Outline each Plasmodium falciparum-infected red blood cell.
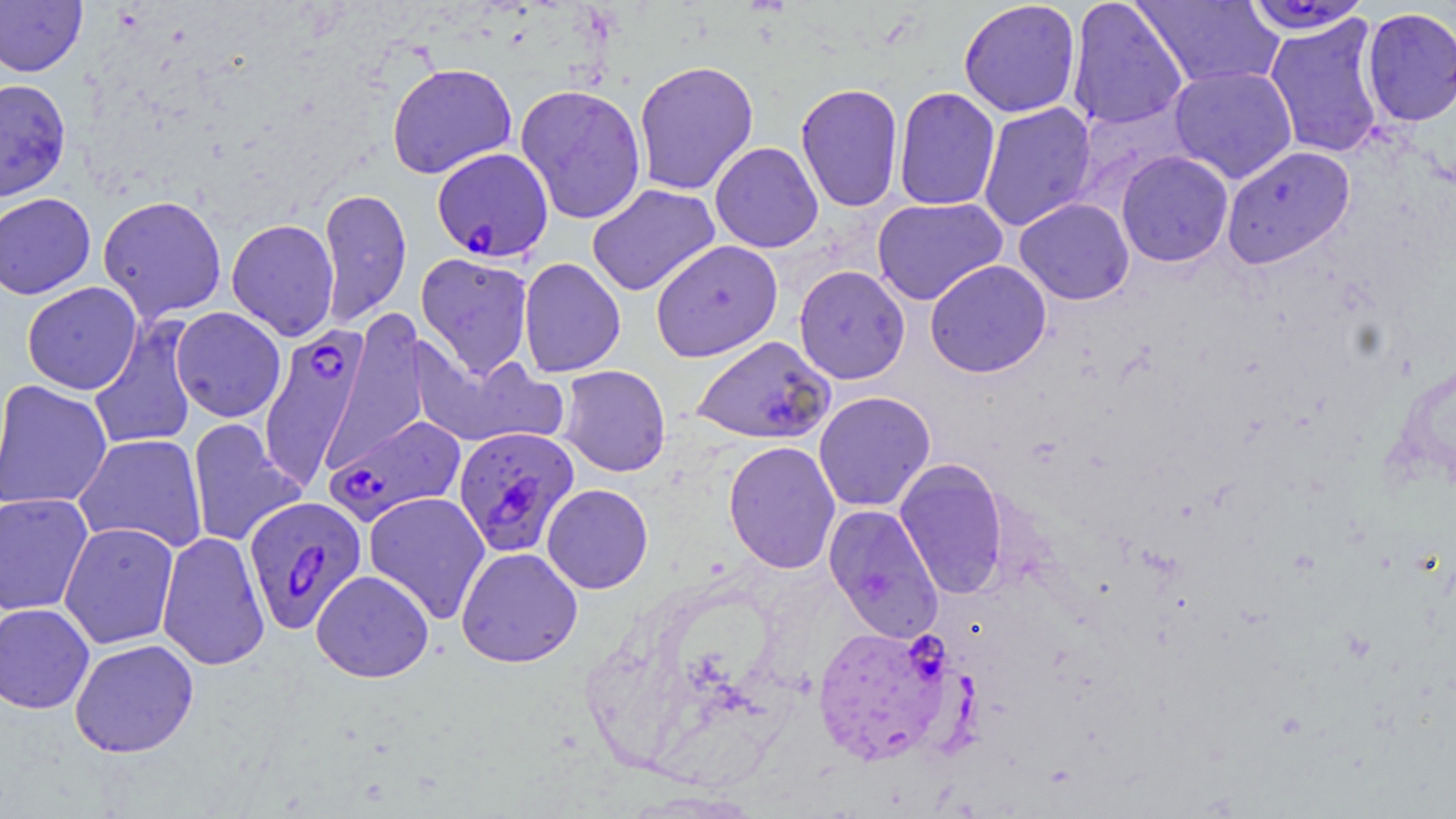

Approximate bounding boxes as named x1/y1/x2/y2 corners in pixels.
Plasmodium falciparum-infected red blood cells: (x1=432, y1=147, x2=554, y2=262), (x1=258, y1=321, x2=371, y2=485), (x1=690, y1=335, x2=835, y2=445), (x1=324, y1=413, x2=466, y2=527), (x1=453, y1=426, x2=580, y2=557), (x1=243, y1=495, x2=368, y2=634), (x1=812, y1=624, x2=954, y2=766).

slide_level_diagnosis: Plasmodium falciparum
image_size: 1456×819 pixels
modality: optical microscopy
uninfected_red_blood_cell_locations: 'approximate bounding boxes as named x1/y1/x2/y2 corners in pixels: (x1=958, y1=0, x2=1081, y2=118), (x1=1066, y1=0, x2=1188, y2=130), (x1=1132, y1=0, x2=1285, y2=89), (x1=0, y1=1, x2=87, y2=76), (x1=1240, y1=1, x2=1374, y2=36), (x1=1360, y1=7, x2=1456, y2=127), (x1=1263, y1=16, x2=1387, y2=158), (x1=633, y1=59, x2=759, y2=196), (x1=387, y1=63, x2=517, y2=179), (x1=1169, y1=66, x2=1297, y2=183), (x1=0, y1=78, x2=71, y2=202), (x1=795, y1=82, x2=903, y2=212), (x1=514, y1=84, x2=647, y2=225), (x1=893, y1=87, x2=1000, y2=211), (x1=977, y1=102, x2=1096, y2=232), (x1=710, y1=141, x2=824, y2=252), (x1=1221, y1=145, x2=1356, y2=268), (x1=1116, y1=151, x2=1234, y2=267), (x1=586, y1=184, x2=720, y2=296), (x1=317, y1=187, x2=412, y2=327), (x1=0, y1=193, x2=96, y2=299), (x1=97, y1=194, x2=227, y2=323), (x1=871, y1=196, x2=1008, y2=305), (x1=1014, y1=198, x2=1134, y2=305), (x1=226, y1=218, x2=340, y2=341), (x1=651, y1=240, x2=783, y2=362), (x1=416, y1=253, x2=534, y2=377), (x1=518, y1=257, x2=626, y2=378), (x1=925, y1=259, x2=1052, y2=378), (x1=793, y1=265, x2=911, y2=384), (x1=22, y1=281, x2=142, y2=395), (x1=170, y1=307, x2=286, y2=422), (x1=88, y1=317, x2=201, y2=451), (x1=411, y1=340, x2=566, y2=450), (x1=558, y1=364, x2=671, y2=477), (x1=0, y1=379, x2=113, y2=511), (x1=813, y1=391, x2=936, y2=512), (x1=186, y1=418, x2=305, y2=548), (x1=73, y1=433, x2=208, y2=553), (x1=723, y1=440, x2=841, y2=574), (x1=894, y1=458, x2=1009, y2=600), (x1=542, y1=484, x2=653, y2=594), (x1=363, y1=491, x2=490, y2=624), (x1=0, y1=493, x2=93, y2=616), (x1=823, y1=504, x2=944, y2=643), (x1=59, y1=521, x2=180, y2=649), (x1=156, y1=530, x2=270, y2=671), (x1=456, y1=547, x2=583, y2=668), (x1=311, y1=570, x2=434, y2=683), (x1=0, y1=603, x2=94, y2=714), (x1=69, y1=639, x2=199, y2=758)'
magnification: 1000x
preparation: thin blood film
stain: May-Grünwald-Giemsa
field_of_view: single